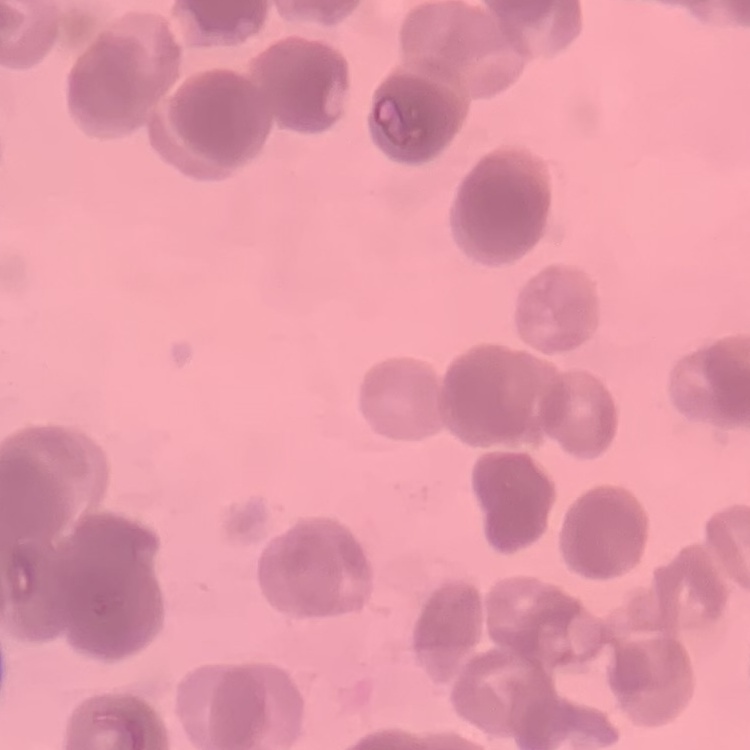
The red blood cells show rouleaux formation. One tile cut from a larger photomicrograph. Thin blood film. Stained with either Field's or Giemsa.